Locate malaria parasites and leukocytes.
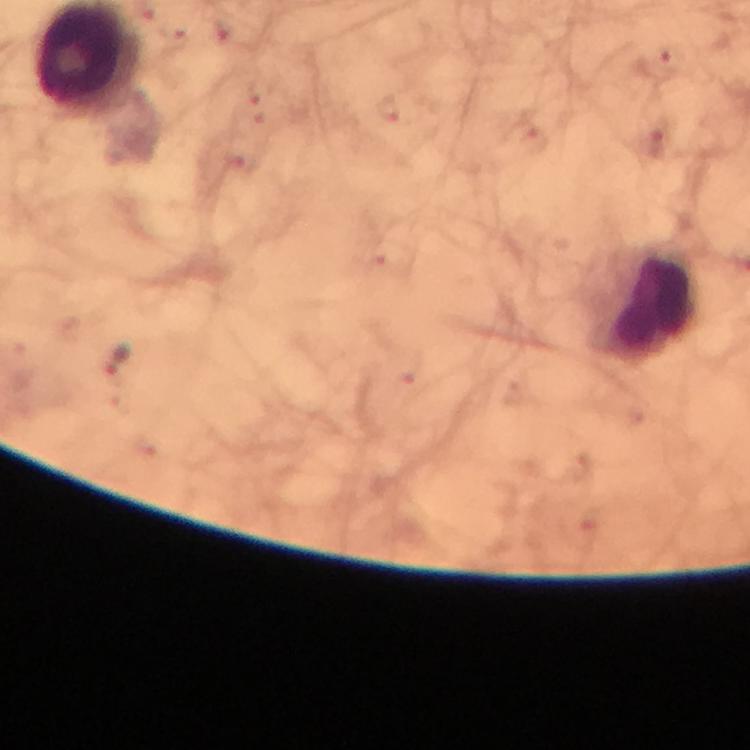
Approximate centers as {x, y} in pixels.
Malaria parasites: {117, 358}.
Leukocytes: {650, 307}.

context: from a malaria diagnostic workup
image_size: 750×750 pixels
preparation: thick smear
magnification: 100x
cropped_from: one field of view
immersion_oil: used
stain: Giemsa
capture: smartphone mounted on the microscope